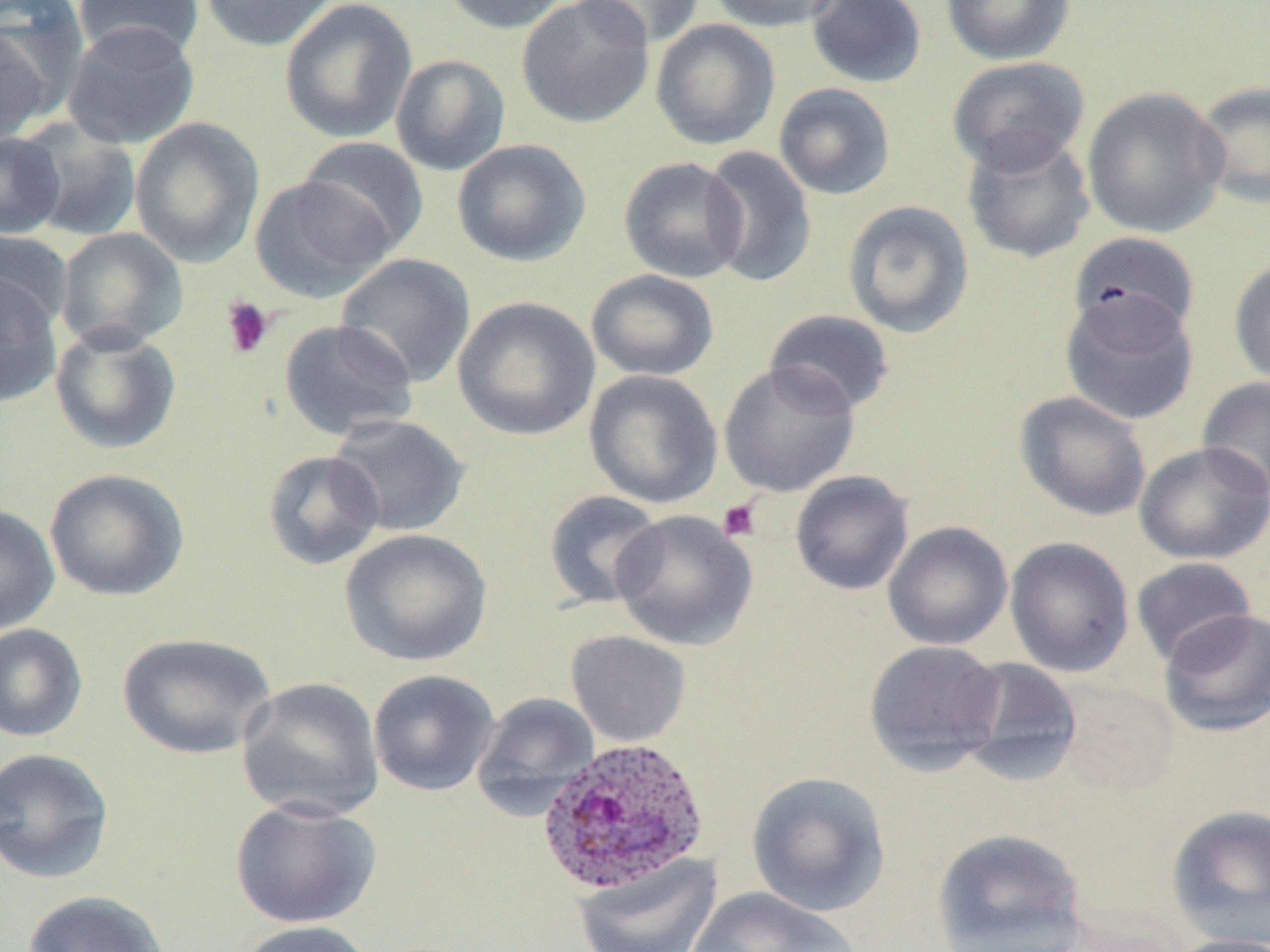
Approximate bounding boxes as (x1, y1, x2, y2) in pixels. Platelet locations: (220, 296, 275, 360), (717, 498, 761, 542). Uninfected red blood cell locations: (73, 0, 204, 63), (199, 0, 340, 52), (279, 0, 417, 143), (439, 0, 571, 35), (516, 0, 655, 128), (571, 0, 705, 49), (707, 0, 844, 33), (805, 0, 927, 89), (940, 0, 1076, 65), (651, 18, 781, 150), (61, 21, 201, 149), (1, 24, 58, 147), (390, 53, 510, 176), (947, 56, 1090, 175), (1191, 80, 1270, 210), (773, 82, 895, 201), (1081, 86, 1230, 238), (130, 117, 265, 268), (20, 120, 142, 242), (0, 130, 66, 239), (960, 130, 1096, 264), (295, 137, 429, 256), (451, 138, 591, 267), (700, 146, 819, 288), (618, 156, 748, 284), (249, 175, 395, 302), (842, 200, 975, 338), (56, 227, 188, 352), (0, 229, 73, 334), (1069, 231, 1201, 342), (335, 253, 476, 388), (1229, 255, 1270, 388), (586, 269, 720, 381), (0, 270, 63, 408), (1059, 289, 1199, 426), (453, 296, 600, 442), (764, 309, 896, 416), (278, 319, 418, 440), (49, 324, 182, 456), (719, 361, 861, 497), (584, 370, 723, 509), (1197, 377, 1270, 498), (1013, 390, 1151, 521), (328, 414, 471, 537), (1134, 441, 1269, 564), (261, 449, 386, 571), (43, 467, 189, 602), (790, 470, 915, 596), (542, 489, 665, 610), (0, 504, 60, 634), (610, 509, 758, 651), (883, 520, 1013, 650), (339, 528, 493, 667), (1004, 536, 1135, 677), (1130, 557, 1258, 667), (1157, 607, 1270, 737), (0, 623, 88, 742), (565, 630, 691, 747), (117, 631, 277, 760), (863, 640, 1007, 775), (952, 656, 1083, 785), (367, 669, 500, 796), (237, 677, 384, 821), (1054, 679, 1182, 796), (471, 692, 599, 819), (0, 746, 115, 884), (745, 771, 891, 917), (230, 797, 381, 929), (1165, 804, 1270, 946), (930, 827, 1089, 952), (573, 853, 722, 951), (685, 887, 860, 952), (22, 889, 171, 952), (234, 920, 377, 952), (1165, 934, 1270, 952). Plasmodium ovale-infected red blood cell locations: (536, 736, 710, 895). Slide-level diagnosis: Plasmodium ovale. Image is 1270×952 pixels. Optical microscopy. One field of a larger specimen. May-Grünwald-Giemsa stain. 1000x magnification. Thin blood film.